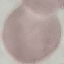

Result: negative for malaria parasites. Thin blood smear. Acquired by smartphone through the microscope eyepiece. Giemsa-stained preparation. Automatically extracted cell patch, resized to 64 × 64 pixels.